Comment on the morphology of the red blood cells.
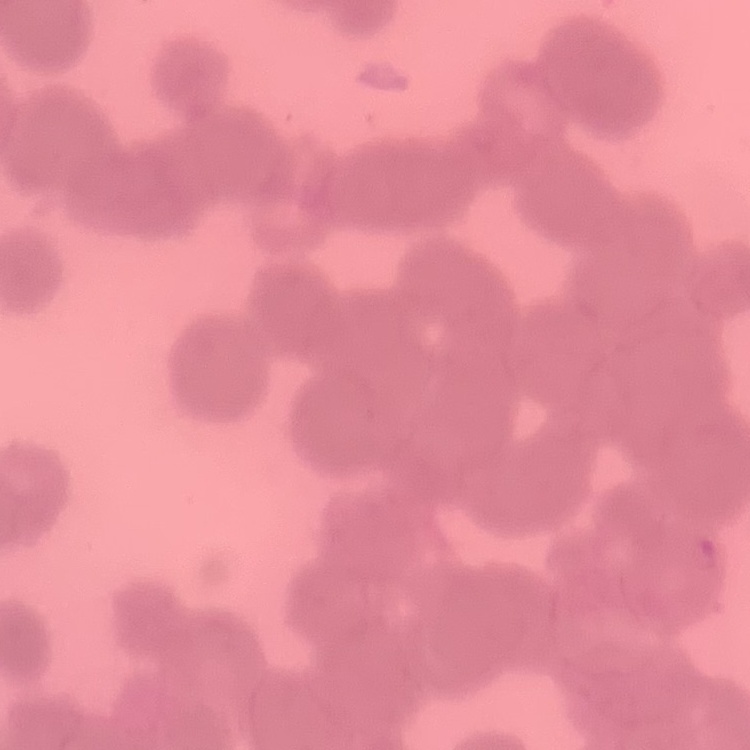

Rouleaux formation.

{
  "stain": "Field's or Giemsa",
  "preparation": "thin blood smear",
  "image_type": "square crop of a larger photomicrograph"
}